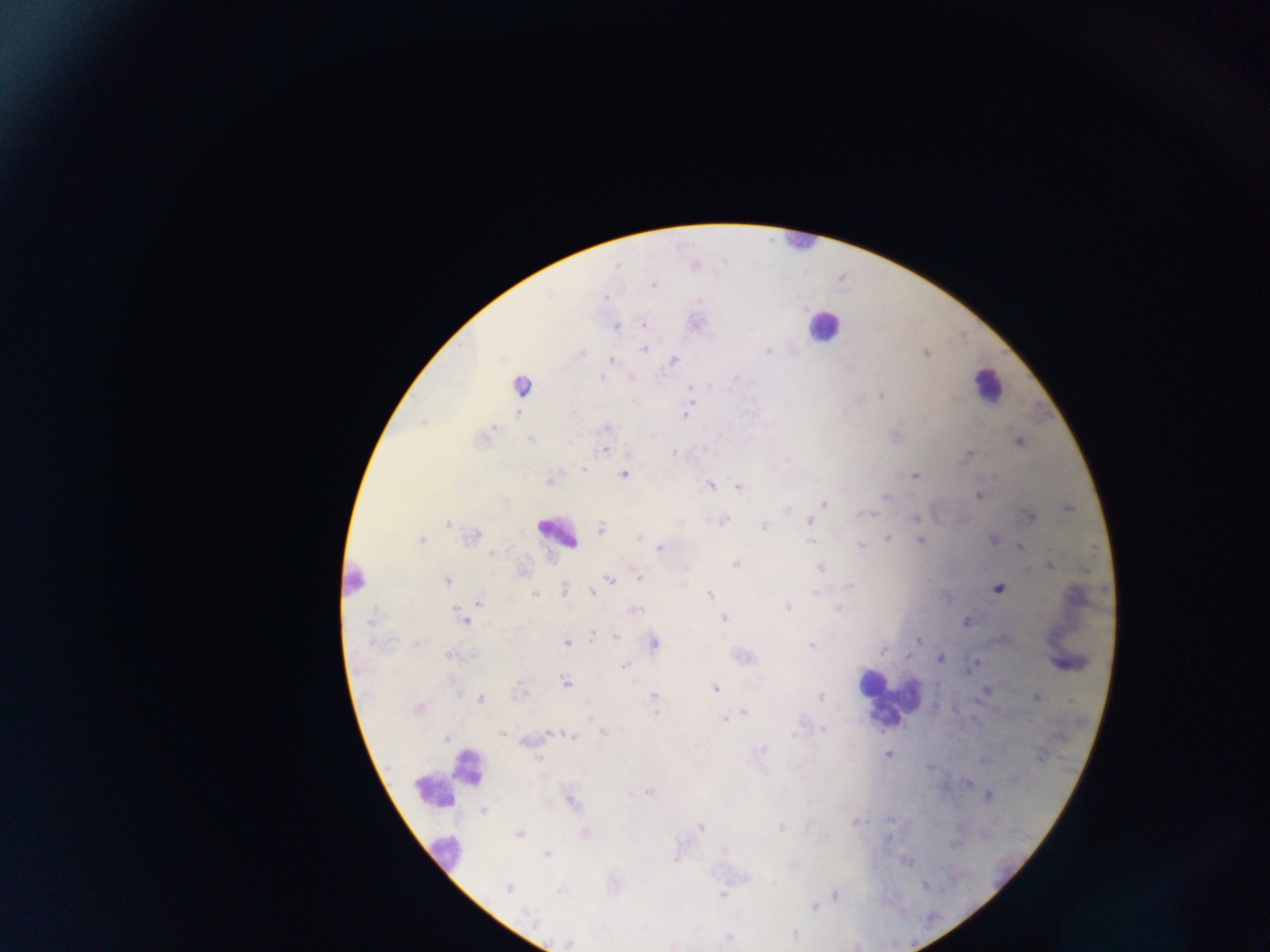
country: Ghana
field_of_view: single
preparation: thick blood smear
malaria_parasite_locations: 'approximate centers as [x, y] in pixels: [653, 285], [606, 297], [643, 324], [616, 327], [643, 349], [767, 350], [925, 353], [582, 354], [611, 360], [673, 360], [601, 378], [521, 385], [689, 389], [882, 395], [518, 413], [685, 415], [494, 427], [607, 427], [531, 439], [1019, 442], [604, 450], [674, 453], [966, 455], [584, 469], [623, 475], [914, 476], [550, 481], [710, 485], [738, 487], [978, 495], [885, 497], [824, 503], [1068, 508], [1030, 516], [915, 517], [724, 520], [809, 521], [448, 523], [764, 526], [601, 529], [472, 536], [888, 538], [992, 539], [420, 540], [811, 541], [921, 541], [861, 546], [1019, 547], [659, 548], [735, 564], [1050, 565], [821, 568], [638, 576], [447, 580], [610, 580], [848, 586], [597, 588], [998, 589], [565, 590], [591, 591], [815, 592], [535, 593], [710, 594], [479, 603], [788, 607], [839, 608], [636, 610], [724, 619], [371, 621], [463, 621], [966, 621], [592, 635], [616, 636], [918, 640], [566, 643], [654, 643], [417, 644], [811, 645], [883, 650], [451, 655], [940, 658], [975, 662], [624, 666], [565, 682], [715, 688], [986, 690], [654, 697], [820, 697], [1036, 698], [481, 699], [418, 707], [655, 712], [743, 713], [724, 719], [823, 729], [550, 733], [603, 733], [504, 734], [571, 736], [447, 738], [763, 749], [887, 755], [648, 792], [989, 795], [572, 801], [483, 811], [855, 822], [701, 827], [780, 827], [519, 833], [585, 834], [547, 854], [507, 888], [836, 894], [722, 896], [813, 906], [527, 913], [569, 943]'
leukocyte_locations: 'approximate centers as [x, y] in pixels: [799, 243], [823, 326], [987, 384], [557, 534], [352, 582], [869, 685], [886, 700], [446, 778], [445, 853]'
image_size: 1270×952 pixels
capture: mobile-phone photograph through a microscope